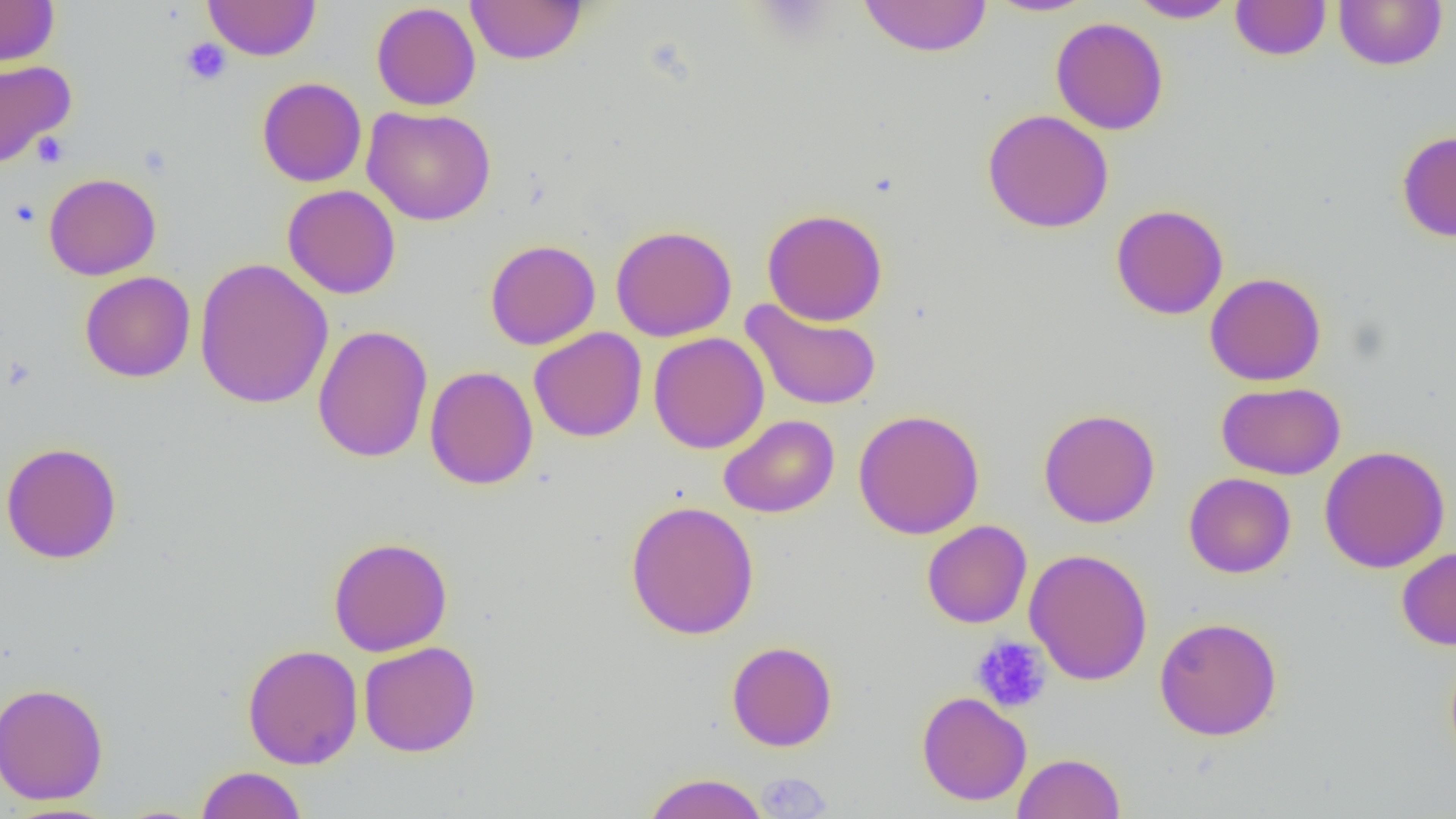
Summary:
  - Coordinate format: approximate bounding boxes as named x1/y1/x2/y2 corners in pixels
  - Platelet locations (subset): (x1=180, y1=38, x2=232, y2=86), (x1=32, y1=133, x2=70, y2=168), (x1=8, y1=199, x2=42, y2=228), (x1=971, y1=635, x2=1052, y2=713)
  - Uninfected red blood cell locations (subset): (x1=0, y1=0, x2=60, y2=67), (x1=204, y1=0, x2=320, y2=61), (x1=466, y1=0, x2=587, y2=65), (x1=858, y1=0, x2=993, y2=57), (x1=985, y1=0, x2=1097, y2=17), (x1=1127, y1=0, x2=1239, y2=23), (x1=1230, y1=0, x2=1331, y2=60), (x1=1333, y1=0, x2=1447, y2=71), (x1=371, y1=2, x2=481, y2=110), (x1=1051, y1=16, x2=1168, y2=135), (x1=0, y1=59, x2=76, y2=168), (x1=256, y1=77, x2=367, y2=187), (x1=362, y1=105, x2=496, y2=226), (x1=982, y1=109, x2=1114, y2=233), (x1=1396, y1=130, x2=1456, y2=242), (x1=43, y1=173, x2=161, y2=280), (x1=282, y1=184, x2=401, y2=299), (x1=1111, y1=204, x2=1228, y2=320), (x1=762, y1=209, x2=888, y2=326), (x1=610, y1=224, x2=738, y2=342), (x1=485, y1=239, x2=600, y2=350), (x1=194, y1=257, x2=334, y2=410), (x1=79, y1=271, x2=196, y2=383), (x1=1205, y1=272, x2=1327, y2=386), (x1=740, y1=298, x2=884, y2=411), (x1=312, y1=324, x2=433, y2=463), (x1=529, y1=327, x2=647, y2=442), (x1=648, y1=331, x2=769, y2=454), (x1=424, y1=365, x2=538, y2=490), (x1=1216, y1=381, x2=1345, y2=480), (x1=1039, y1=408, x2=1160, y2=528), (x1=853, y1=409, x2=985, y2=539), (x1=718, y1=414, x2=840, y2=518), (x1=1, y1=441, x2=123, y2=564), (x1=1320, y1=445, x2=1451, y2=574), (x1=1183, y1=472, x2=1296, y2=578), (x1=625, y1=499, x2=760, y2=640), (x1=922, y1=520, x2=1032, y2=628), (x1=328, y1=536, x2=453, y2=656), (x1=1396, y1=546, x2=1456, y2=651), (x1=1024, y1=548, x2=1153, y2=686), (x1=1154, y1=616, x2=1282, y2=740), (x1=359, y1=641, x2=481, y2=757), (x1=726, y1=641, x2=838, y2=752), (x1=242, y1=643, x2=363, y2=769), (x1=0, y1=682, x2=109, y2=805), (x1=916, y1=690, x2=1032, y2=806), (x1=1013, y1=752, x2=1125, y2=819), (x1=196, y1=766, x2=307, y2=819), (x1=643, y1=772, x2=769, y2=819), (x1=0, y1=802, x2=123, y2=819)
  - Slide-level diagnosis: negative for blood parasites
  - Preparation: thin blood smear
  - Image size: 1456×819 pixels
  - Modality: optical microscopy
  - Field of view: one of a larger specimen
  - Magnification: 1000x